Point out each Plasmodium parasite.
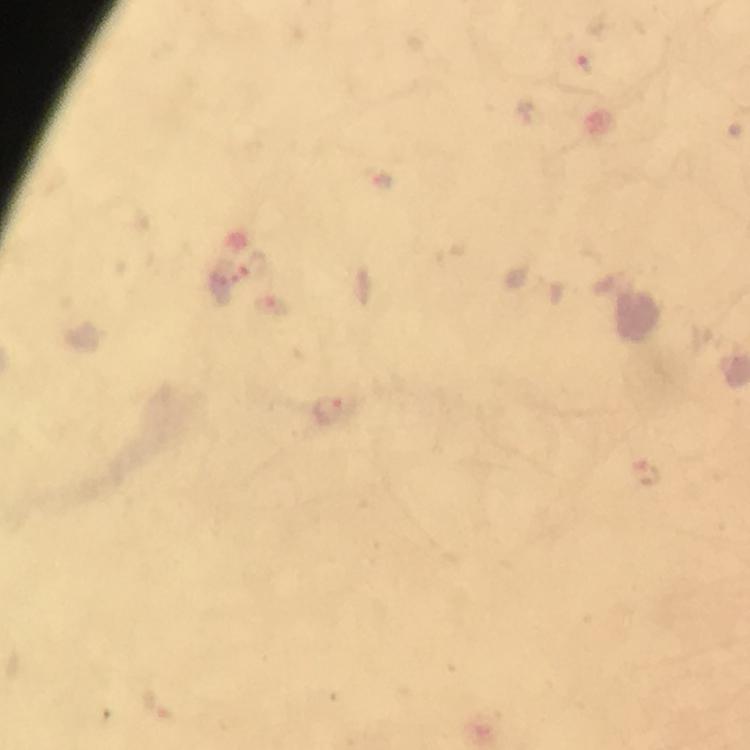

Approximate centers as {x, y} in pixels.
Plasmodium parasites: {588, 62}, {328, 411}, {647, 472}.

Thick blood film. Immersion oil applied. At 100x magnification. Image is 750×750 pixels. Cropped region of a single field of view. From a diagnostic examination for malaria. Photographed through the microscope with a smartphone camera. Giemsa stain.